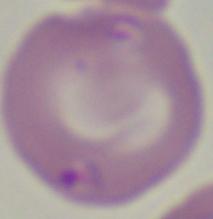 A Babesia parasite is seen. Photomicrograph. 1000x magnification.